Describe the morphology of the red blood cells.
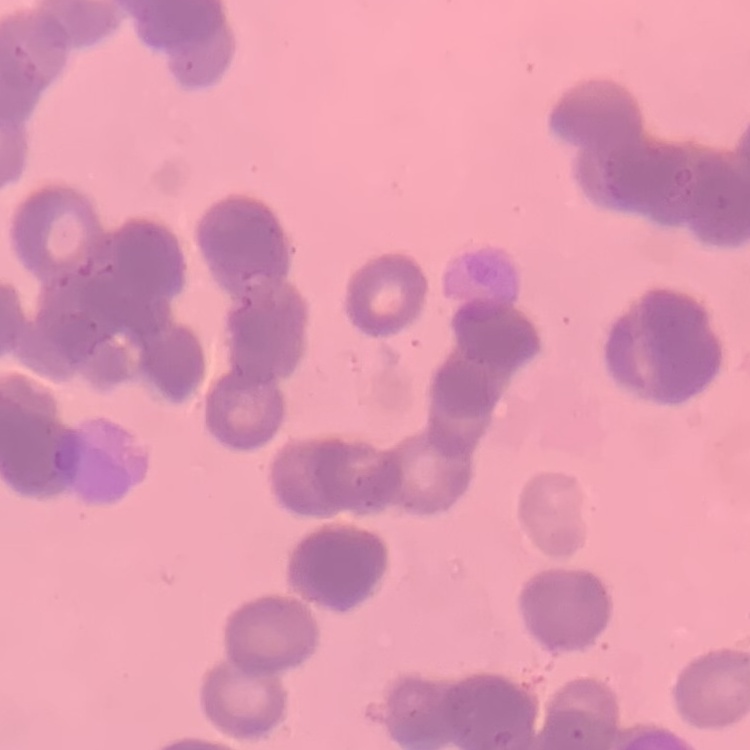
Rouleaux formation.

Summary:
  - Image type: square crop of a larger photomicrograph
  - Preparation: thin blood smear
  - Stain: Field's or Giemsa